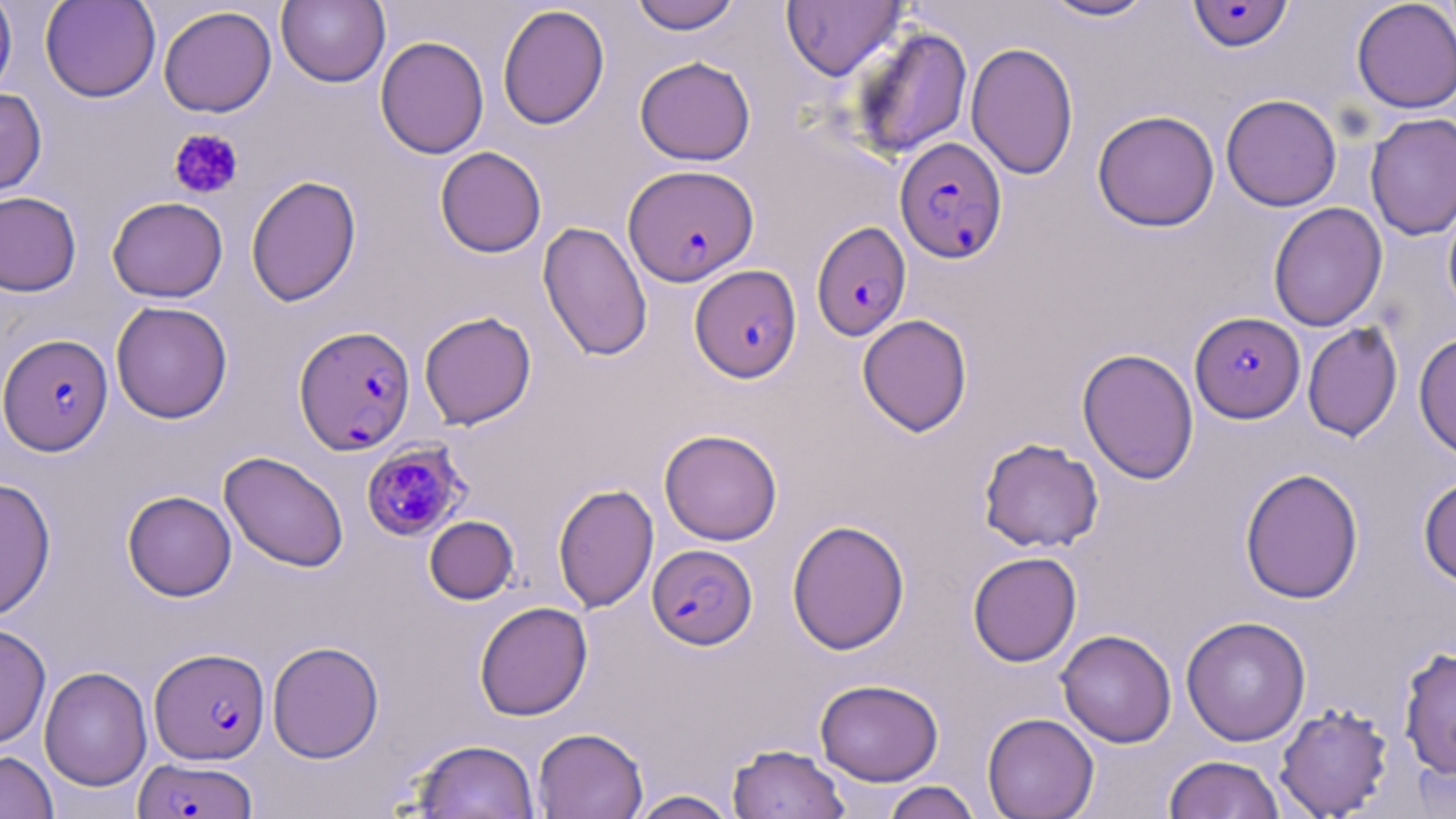

Approximate bounding boxes as (x1,y1)-(x2,y2) corner pairs in pixels. Plasmodium falciparum-infected red blood cell locations: (1187,1)-(1294,52), (895,137)-(1008,263), (623,164)-(759,286), (811,220)-(912,340), (689,265)-(802,383), (1190,311)-(1305,423), (293,326)-(415,455), (1,334)-(113,455), (361,442)-(468,541), (647,544)-(757,650), (148,647)-(270,765), (134,757)-(258,818). Platelet locations: (168,128)-(244,200). Uninfected red blood cell locations: (0,0)-(17,101), (39,0)-(161,102), (276,0)-(390,87), (629,0)-(743,34), (1038,0)-(1158,22), (1351,0)-(1456,113), (781,1)-(907,81), (497,4)-(610,130), (157,5)-(277,117), (846,24)-(973,160), (375,35)-(490,159), (965,42)-(1079,180), (634,56)-(756,166), (0,87)-(47,198), (1221,93)-(1342,211), (1092,110)-(1220,232), (1365,112)-(1456,241), (435,146)-(547,258), (245,175)-(362,306), (0,190)-(82,296), (1442,195)-(1456,320), (107,196)-(228,302), (1268,202)-(1387,331), (537,221)-(653,362), (110,300)-(233,424), (418,311)-(537,430), (857,314)-(973,436), (1302,321)-(1403,441), (1413,332)-(1456,461), (1077,347)-(1199,484), (659,428)-(783,546), (978,437)-(1104,553), (219,451)-(349,572), (1239,467)-(1364,604), (1418,473)-(1456,589), (0,478)-(56,620), (552,483)-(659,613), (122,490)-(237,601), (424,515)-(519,604), (787,519)-(910,655), (967,551)-(1082,667), (474,601)-(593,721), (1181,615)-(1311,746), (0,623)-(51,750), (1056,629)-(1177,748), (267,641)-(384,763), (1397,646)-(1456,779), (39,666)-(152,792), (814,678)-(944,786), (1274,702)-(1394,818), (982,712)-(1100,819), (532,727)-(648,819), (409,738)-(540,819), (727,742)-(850,819), (0,749)-(59,819), (1163,754)-(1286,819), (880,781)-(982,819), (628,790)-(740,819). Slide-level diagnosis: Plasmodium falciparum. Captured at 1000x magnification. May-Grünwald-Giemsa stain. Image is 1456×819 pixels. Single field of view. Optical microscopy. Thin blood smear.